Report the malaria status of this cell.
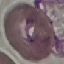
Uninfected.

{
  "image_type": "cell patch, automatically extracted from a larger field of view and resized to 64 × 64 pixels",
  "capture": "smartphone through the microscope eyepiece",
  "preparation": "thin blood film",
  "stain": "Giemsa"
}